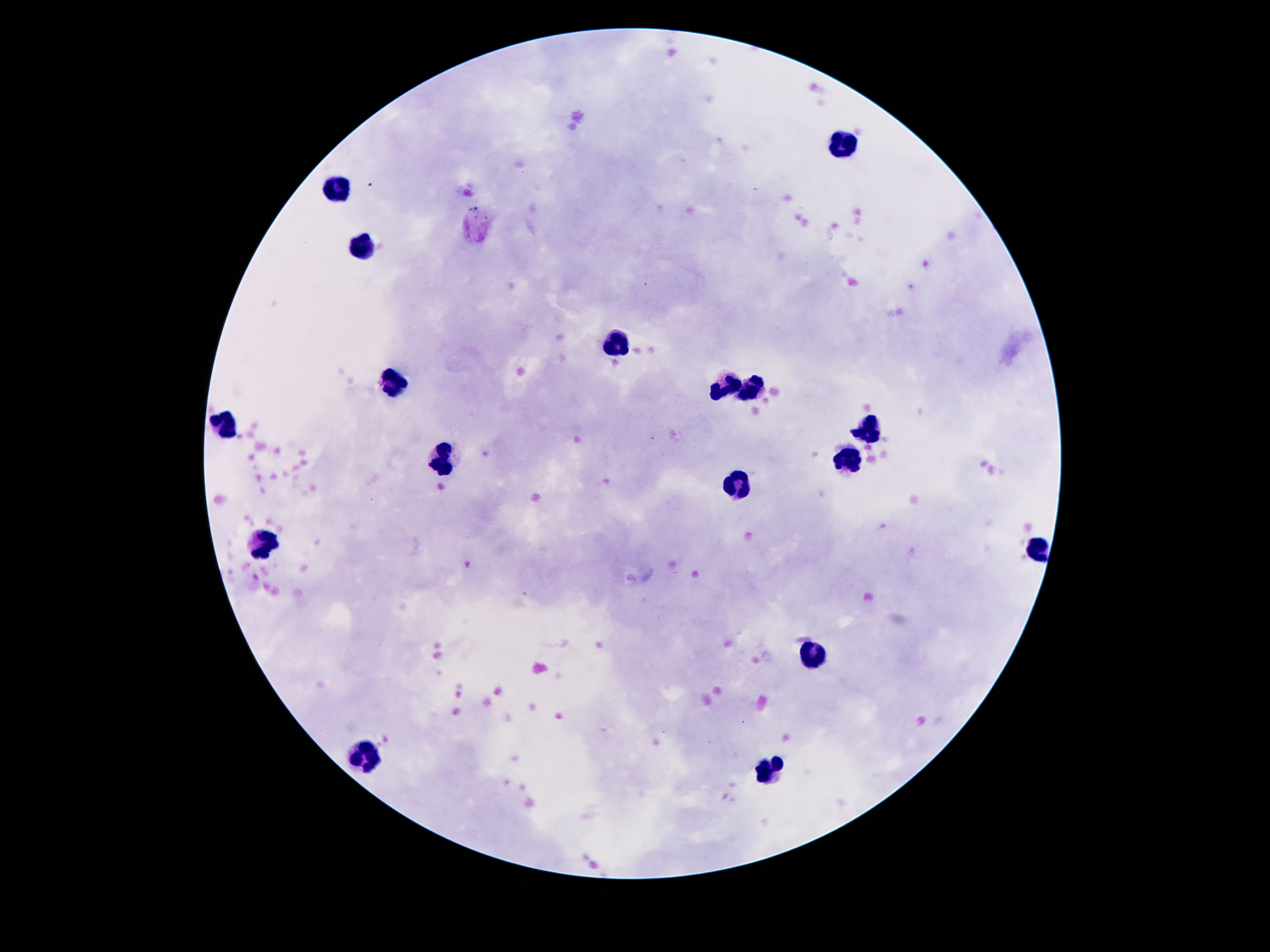

Approximate centers as (x, y) in pixels.
Summary:
  - Leukocyte locations: (843, 143), (341, 186), (362, 244), (616, 341), (397, 386), (722, 386), (756, 388), (226, 423), (869, 429), (849, 461), (444, 462), (735, 485), (267, 543), (1039, 551), (815, 653), (362, 756), (769, 771)
  - Preparation: thick peripheral-blood smear
  - Image size: 1270×952 pixels
  - Capture: smartphone camera through the microscope eyepiece
  - Stain: Giemsa
  - Magnification: 100x
  - Patient malaria status: negative
  - Field of view: single